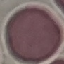
result = no malaria parasites detected
capture = smartphone through the microscope eyepiece
image type = cell patch, automatically extracted from a larger field of view and resized to 64 × 64 pixels
stain = Giemsa
preparation = thin blood smear